Report the malaria status of this cell.
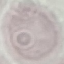
It is uninfected.

Summary:
  - Preparation: thin smear
  - Capture: smartphone through the microscope eyepiece
  - Image type: cell patch, automatically extracted from a larger field of view and resized to 64 × 64 pixels
  - Stain: Giemsa